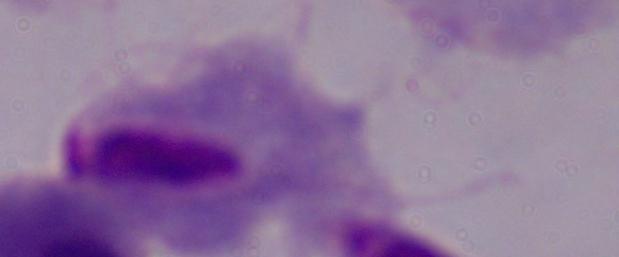
Summary:
  - Identification: trichomonad
  - Magnification: 1000x
  - Modality: photomicrograph